Assess the background quality.
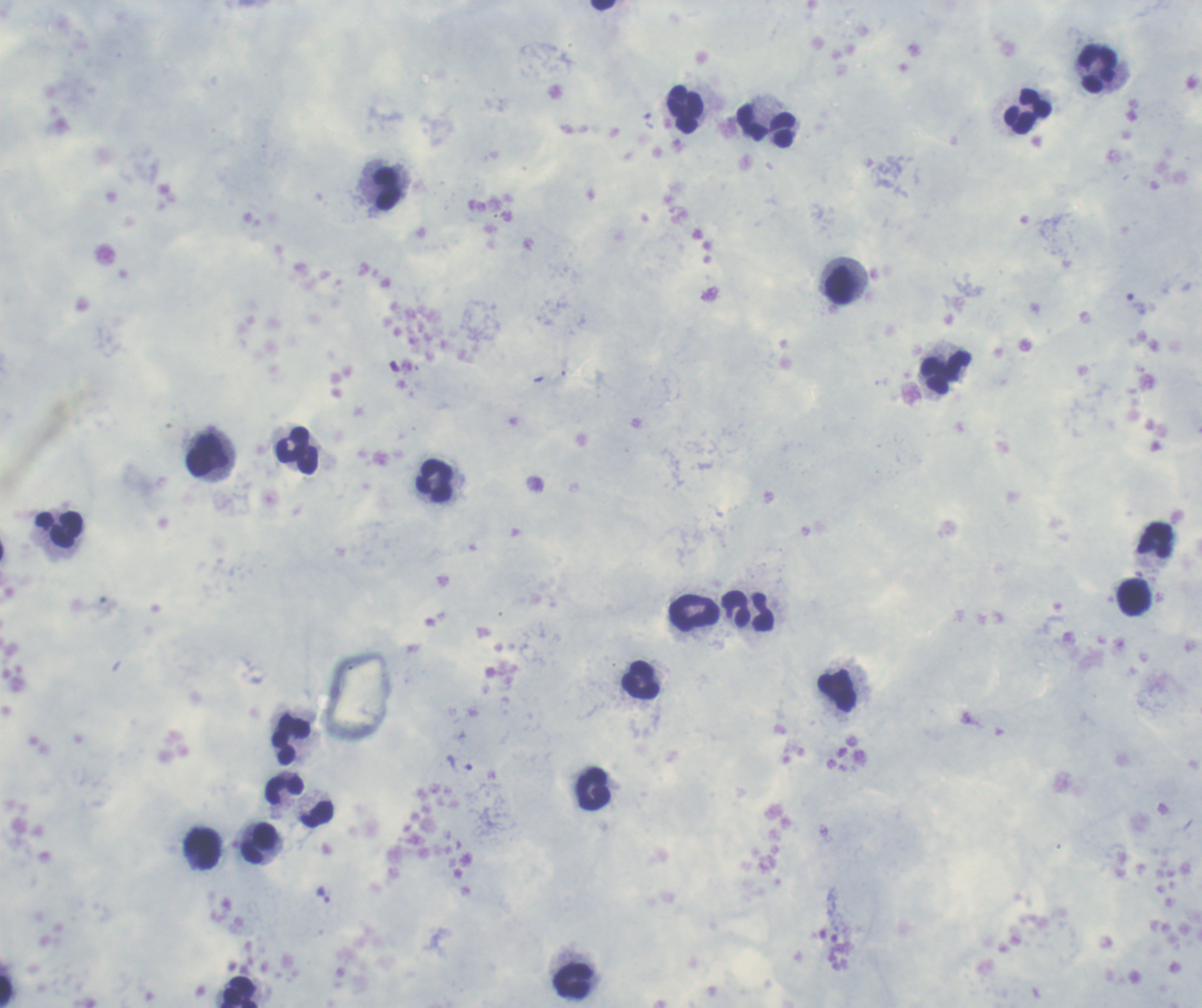

Satisfactory.

Approximate centers as (x, y) in pixels.
Summary:
  - Trophozoite locations: (649, 122), (1136, 305), (459, 765), (323, 894)
  - Leukocyte locations: (602, 5), (1097, 69), (684, 109), (1026, 112), (752, 122), (784, 129), (386, 190), (839, 285), (946, 372), (297, 452), (208, 456), (435, 480), (59, 529), (1157, 541), (737, 609), (695, 614), (763, 614), (640, 682), (838, 691), (291, 740), (593, 789), (285, 790), (316, 814), (259, 844), (202, 848), (573, 980), (7, 991), (241, 992)
  - Coloration quality: good
  - Stain: Romanowsky
  - Context: previously used in a real diagnosis
  - Image size: 1202×1008 pixels
  - Field of view: single
  - Result: positive for Plasmodium parasites
  - Magnification: 100x
  - Preparation: thick blood film